Give the position of every Plasmodium parasite.
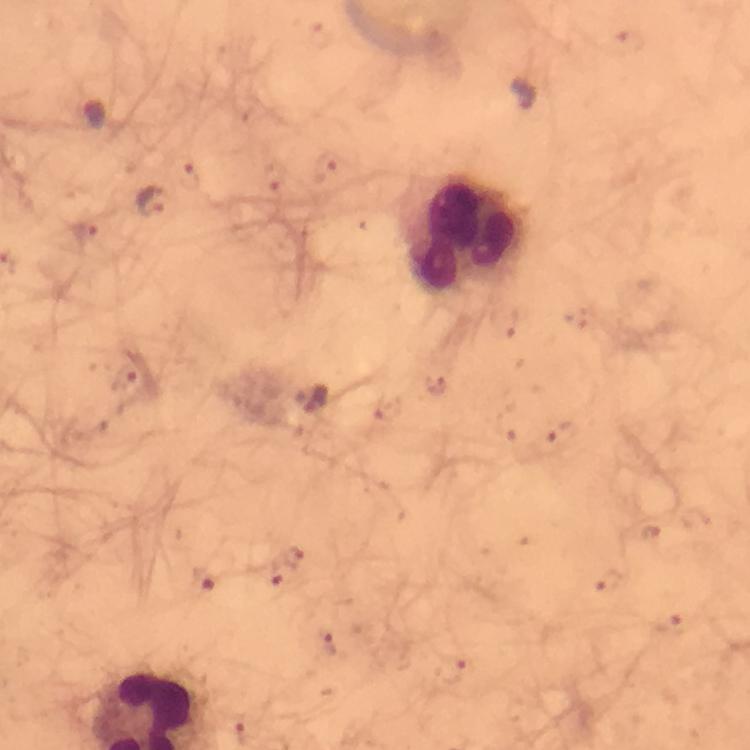
Approximate centers as {x, y} in pixels.
Plasmodium parasites: {629, 42}, {326, 168}, {191, 177}, {273, 178}, {151, 204}, {87, 228}, {124, 379}, {564, 435}, {651, 535}, {294, 557}, {275, 570}, {205, 579}, {609, 583}, {671, 622}, {329, 643}, {450, 669}, {245, 730}.

leukocyte_locations: 'approximate centers as {x, y} in pixels: {462, 235}'
capture: smartphone photograph through a microscope
magnification: 100x
cropped_from: a single field of view
context: from a diagnostic examination for malaria
preparation: thick blood smear
immersion_oil: used
image_size: 750×750 pixels
stain: Giemsa